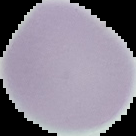

Summary:
  - Preparation: thin blood smear
  - Image size: 136×136 pixels
  - Image type: segmented cell region with the area outside set to black
  - Result: no Plasmodium parasites detected